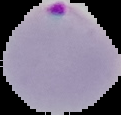
Summary:
  - Image type: segmented cell region on a black background
  - Image size: 121×115 pixels
  - Preparation: thin blood film
  - Malaria status: parasitized